Identify the preparation type.
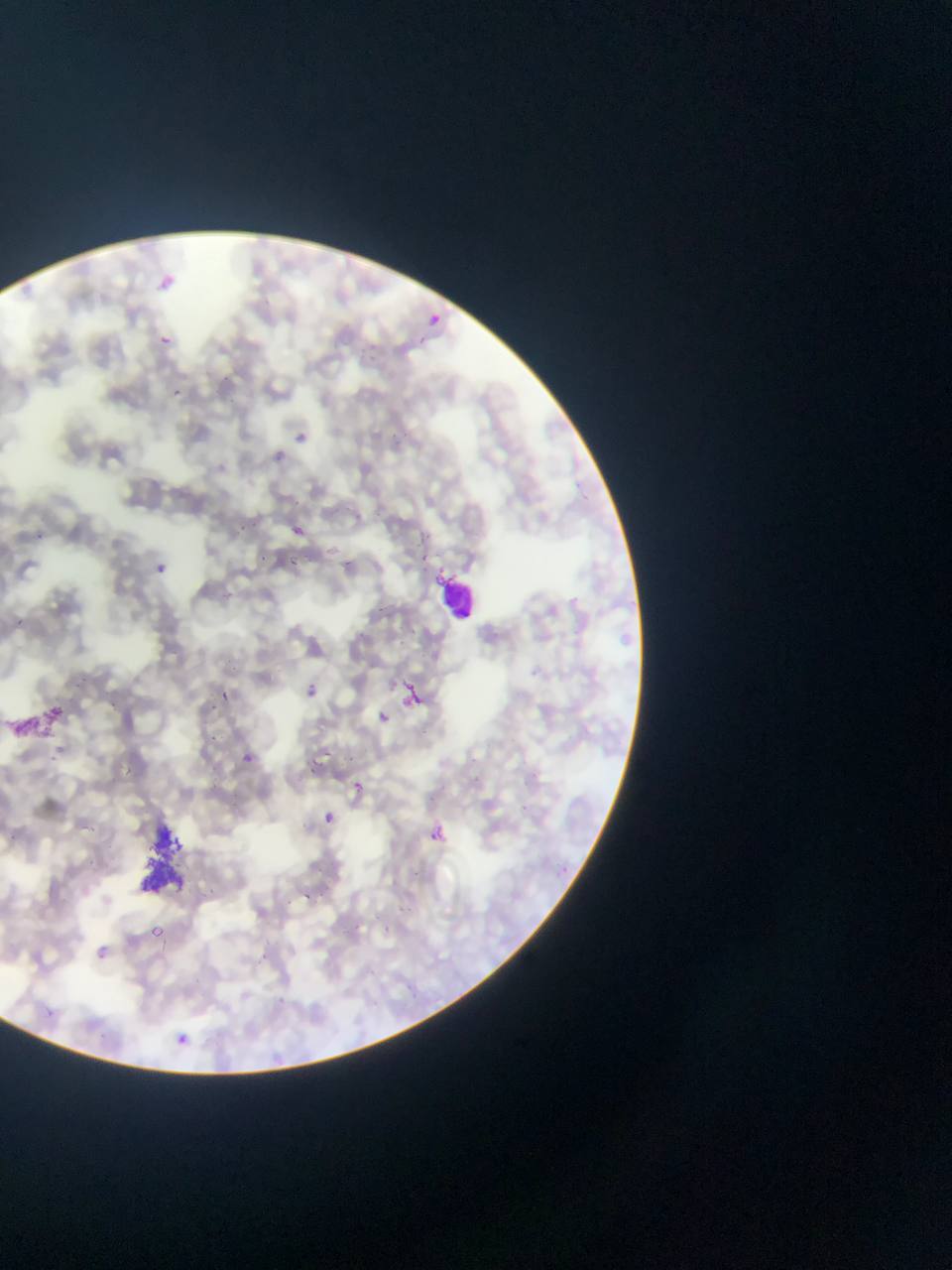

Thin blood film.

capture: mobile-phone photograph through a microscope
country: Ghana
artifact_stain_precipitate_or_debris_locations: 'approximate bounding boxes as [left, top, right, bottom] in pixels: [4, 694, 82, 766], [136, 810, 215, 899]'
plasmodium_parasite_locations: 'approximate bounding boxes as [left, top, right, bottom] in pixels: [418, 308, 446, 334], [156, 333, 173, 349], [174, 387, 182, 401], [293, 497, 307, 508], [287, 521, 308, 541], [235, 523, 245, 532], [39, 531, 51, 544], [423, 553, 429, 562], [258, 554, 267, 562], [149, 558, 173, 579], [289, 558, 300, 566], [223, 589, 233, 602], [374, 600, 391, 616], [17, 617, 27, 627], [393, 680, 429, 714], [302, 683, 322, 701], [215, 688, 233, 704], [110, 699, 116, 711], [370, 708, 394, 731], [207, 733, 217, 745], [325, 747, 335, 757], [245, 751, 253, 764], [312, 755, 320, 764], [125, 764, 140, 781], [310, 769, 319, 777], [345, 776, 369, 797], [320, 810, 339, 828], [424, 821, 452, 849], [555, 860, 574, 878], [303, 889, 314, 900], [145, 922, 168, 943], [383, 928, 391, 935], [47, 1006, 52, 1018], [164, 1027, 196, 1055]'
object_labeled_both_plasmodium_parasite_and_leukocyte_by_the_source: 'approximate bounding boxes as [left, top, right, bottom] in pixels: [436, 568, 480, 623]'
image_size: 952×1270 pixels
field_of_view: single